Comment on the morphology of the erythrocytes.
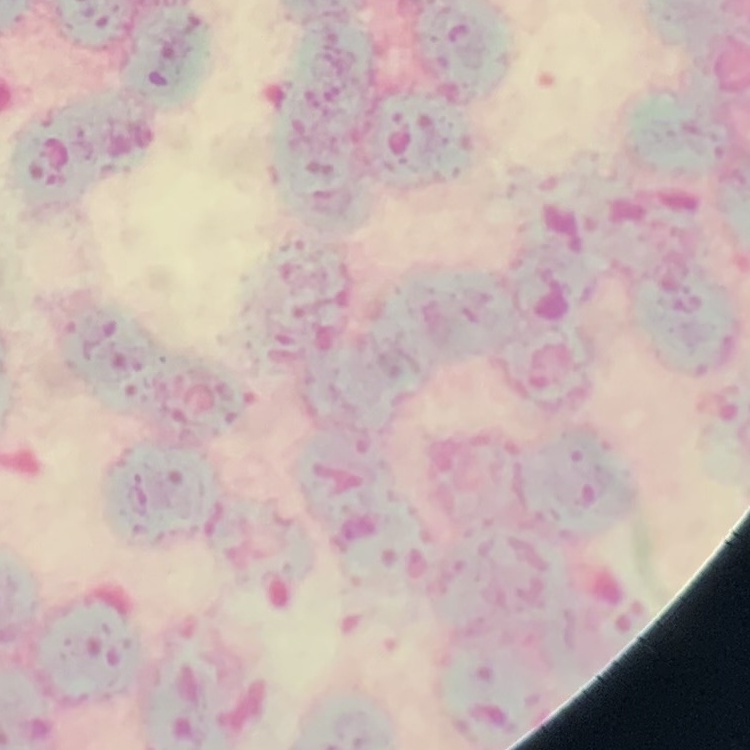

Rouleaux formation.

Thin blood smear. Square crop of a larger photomicrograph. Stained with either Field's or Giemsa.